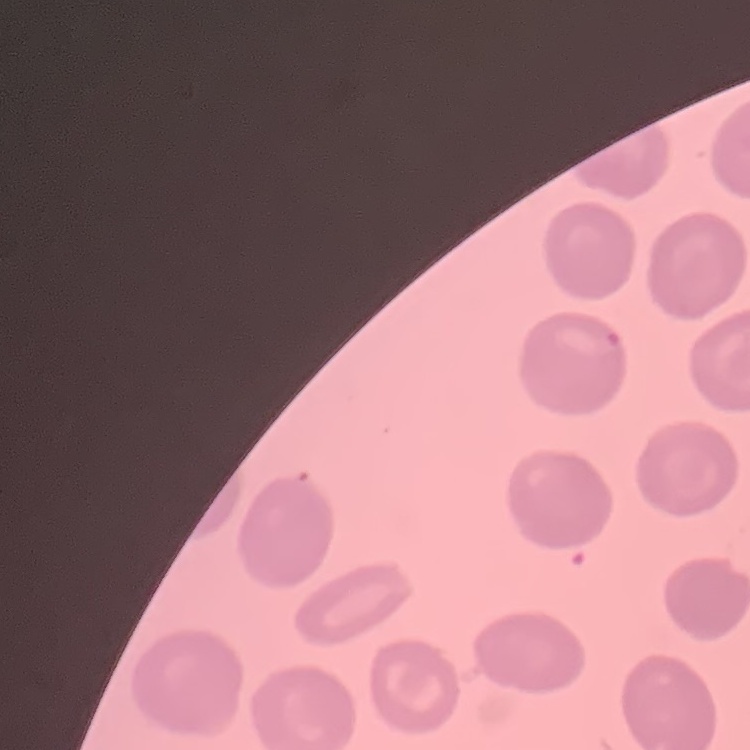
The red blood cells show no rouleaux formation. Thin blood smear. Field's or Giemsa stain. One tile cut from a larger photomicrograph.